Identify the parasite.
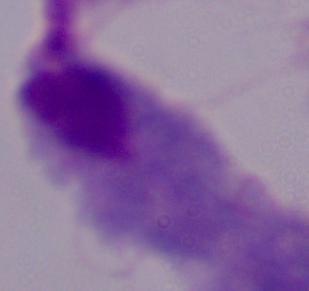
A trichomonad.

Photomicrograph. Captured at 1000x magnification.